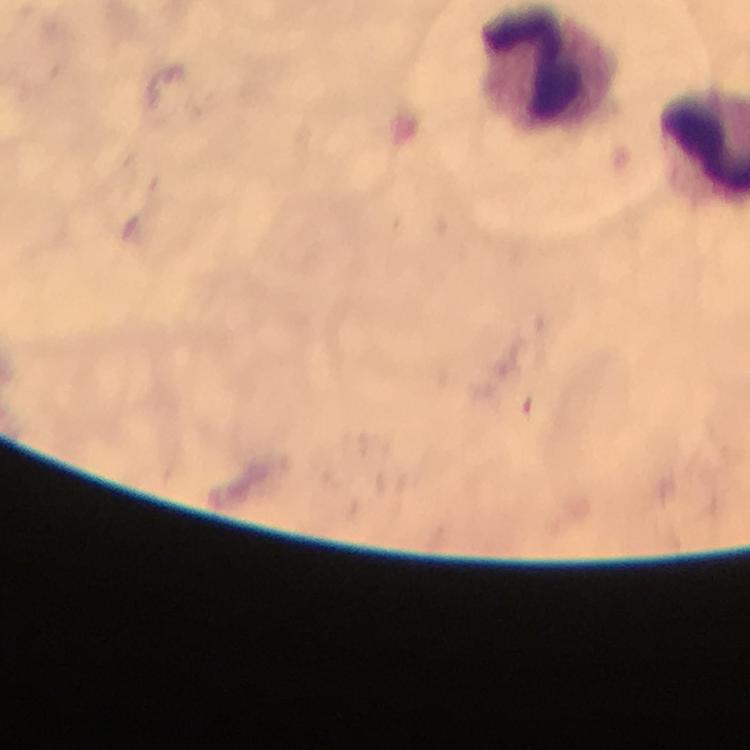
capture = smartphone mounted on the microscope
cropped from = a single field of view
stain = Giemsa
image size = 750×750 pixels
magnification = 100x
context = from a malaria diagnostic workup
leukocyte locations = approximate centers as [x, y] in pixels: [546, 67]
preparation = thick blood film
immersion oil = applied
malaria parasites = none detected